Report the malaria status of this cell.
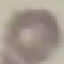

It is uninfected.

image_type: cell patch, automatically extracted from a larger field of view and resized to 64 × 64 pixels
preparation: thin blood film
stain: Giemsa
capture: smartphone through the microscope eyepiece